Assess this cell for malaria.
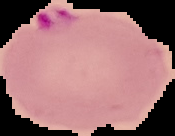

Parasitized.

Summary:
  - Image type: segmented cell region on a black background
  - Image size: 175×136 pixels
  - Preparation: thin blood film